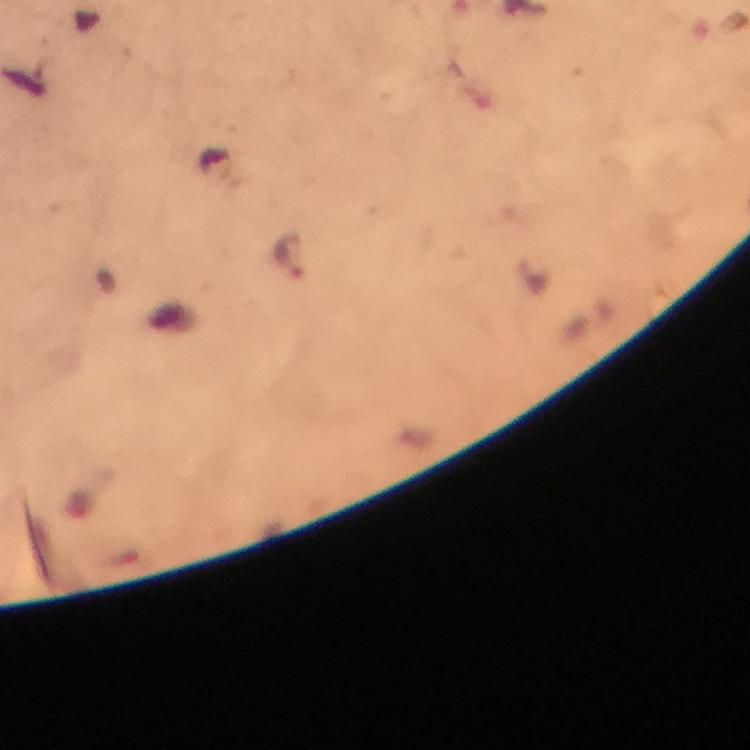
context = from a diagnostic examination for malaria
immersion oil = used
stain = Giemsa
image size = 750×750 pixels
preparation = thick blood smear
capture = smartphone photograph through a microscope
malaria parasite locations = approximate centers as {x, y} in pixels: {289, 256}
cropped from = a single field of view
magnification = 100x